Report the malaria status.
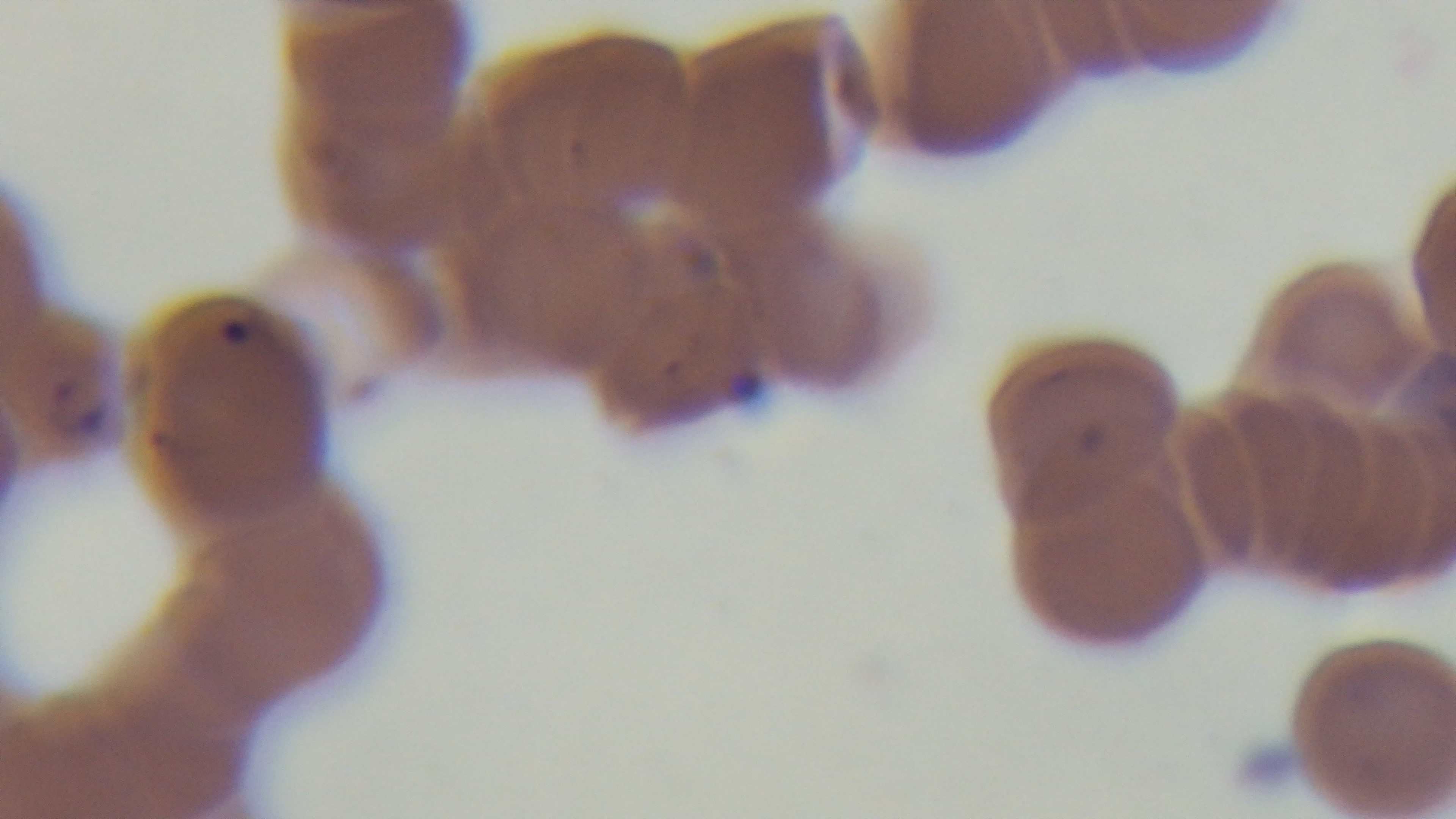

Positive.

preparation: thin blood film
objective: 100x oil immersion
capture: mounted 4K digital camera
field_of_view: single
modality: light microscopy
stain: Giemsa